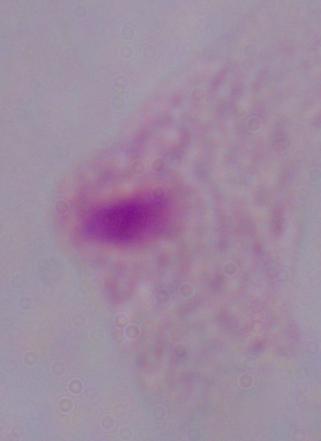

Micrograph. Captured at 1000x magnification. A trichomonad is seen.